Give the extent of all Plasmodium ovale-infected red blood cells.
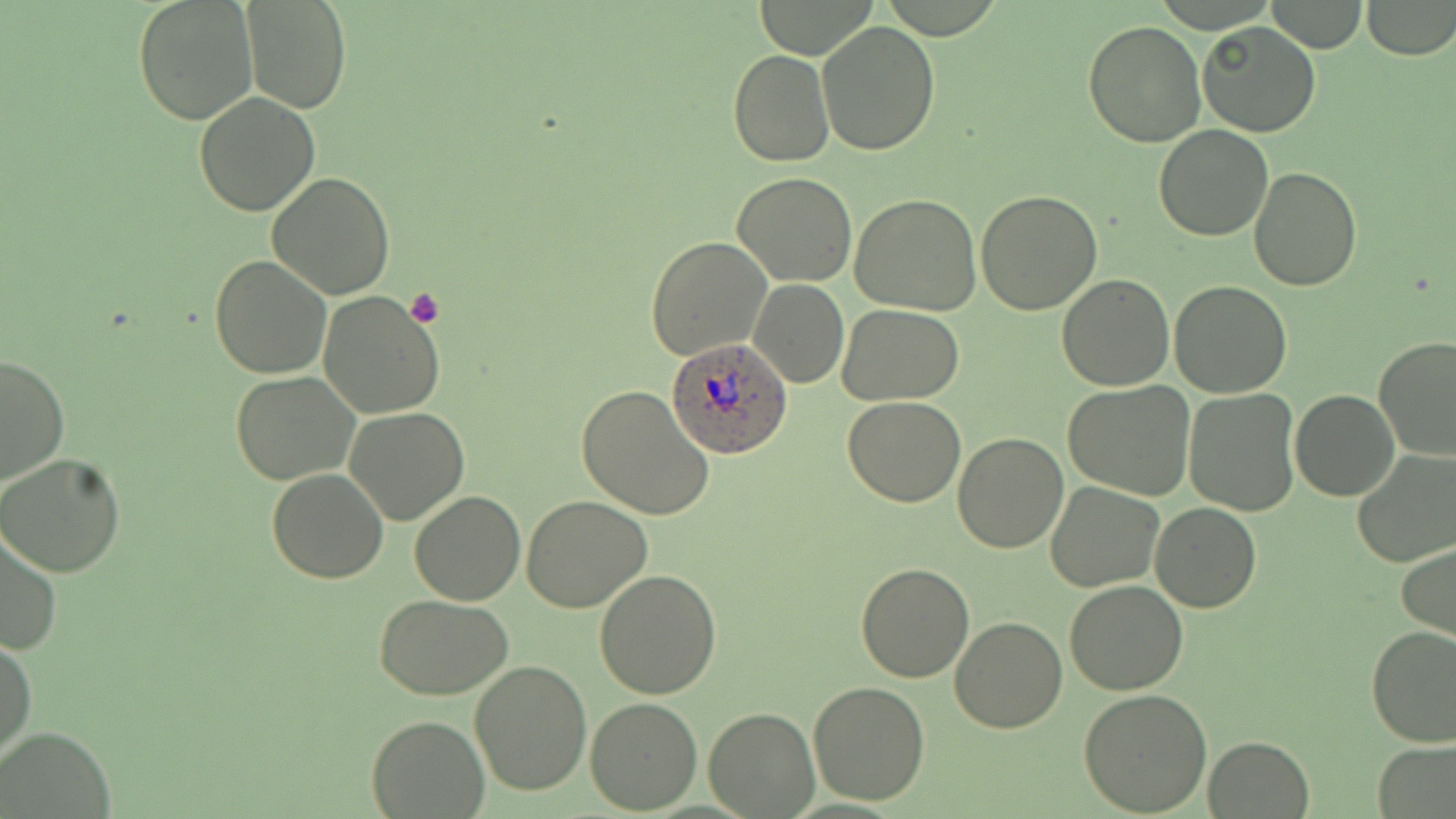
Approximate bounding boxes as (x1, y1, x2, y2) in pixels.
Plasmodium ovale-infected red blood cells: (666, 338, 790, 459).

Platelet locations: (405, 289, 444, 329). Uninfected red blood cell locations: (133, 0, 257, 124), (1266, 0, 1366, 53), (1360, 0, 1455, 58), (242, 1, 349, 114), (816, 19, 942, 156), (1084, 20, 1206, 148), (1198, 21, 1321, 138), (729, 49, 834, 167), (193, 91, 319, 217), (1155, 124, 1273, 241), (1247, 167, 1362, 292), (267, 172, 397, 300), (732, 173, 857, 288), (977, 190, 1104, 314), (850, 193, 981, 314), (646, 238, 771, 359), (210, 255, 332, 379), (1056, 274, 1176, 391), (748, 278, 848, 388), (1170, 281, 1293, 399), (317, 291, 445, 419), (837, 304, 964, 405), (1372, 336, 1456, 462), (0, 355, 69, 488), (230, 371, 360, 485), (1063, 382, 1195, 499), (574, 383, 716, 522), (1184, 388, 1301, 515), (1289, 388, 1399, 501), (843, 397, 966, 507), (344, 407, 469, 525), (953, 432, 1068, 552), (1350, 446, 1456, 566), (0, 452, 127, 577), (266, 469, 389, 584), (1046, 481, 1163, 592), (409, 490, 526, 605), (522, 495, 653, 613), (1151, 503, 1260, 614), (0, 525, 62, 657), (1397, 543, 1456, 642), (856, 562, 974, 681), (594, 569, 723, 699), (1063, 582, 1187, 695), (375, 595, 515, 700), (951, 616, 1066, 732), (1367, 626, 1456, 746), (0, 635, 36, 767), (470, 660, 594, 796), (807, 680, 929, 806), (1080, 688, 1212, 814), (586, 697, 702, 814), (703, 706, 819, 817), (365, 714, 489, 817), (2, 725, 115, 817), (1204, 735, 1315, 817), (1374, 742, 1456, 817). Slide-level diagnosis: Plasmodium ovale. Thin blood film. 1000x magnification. May-Grünwald-Giemsa stain. One field of a larger specimen. Light microscopy. Image is 1456×819 pixels.